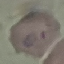

Summary:
  - Malaria status: parasitized
  - Capture: smartphone camera at the microscope eyepiece
  - Preparation: thin blood smear
  - Image type: automatically extracted cell patch, resized to 64 × 64 pixels
  - Stain: Giemsa